Give the extent of all uninfected red blood cells.
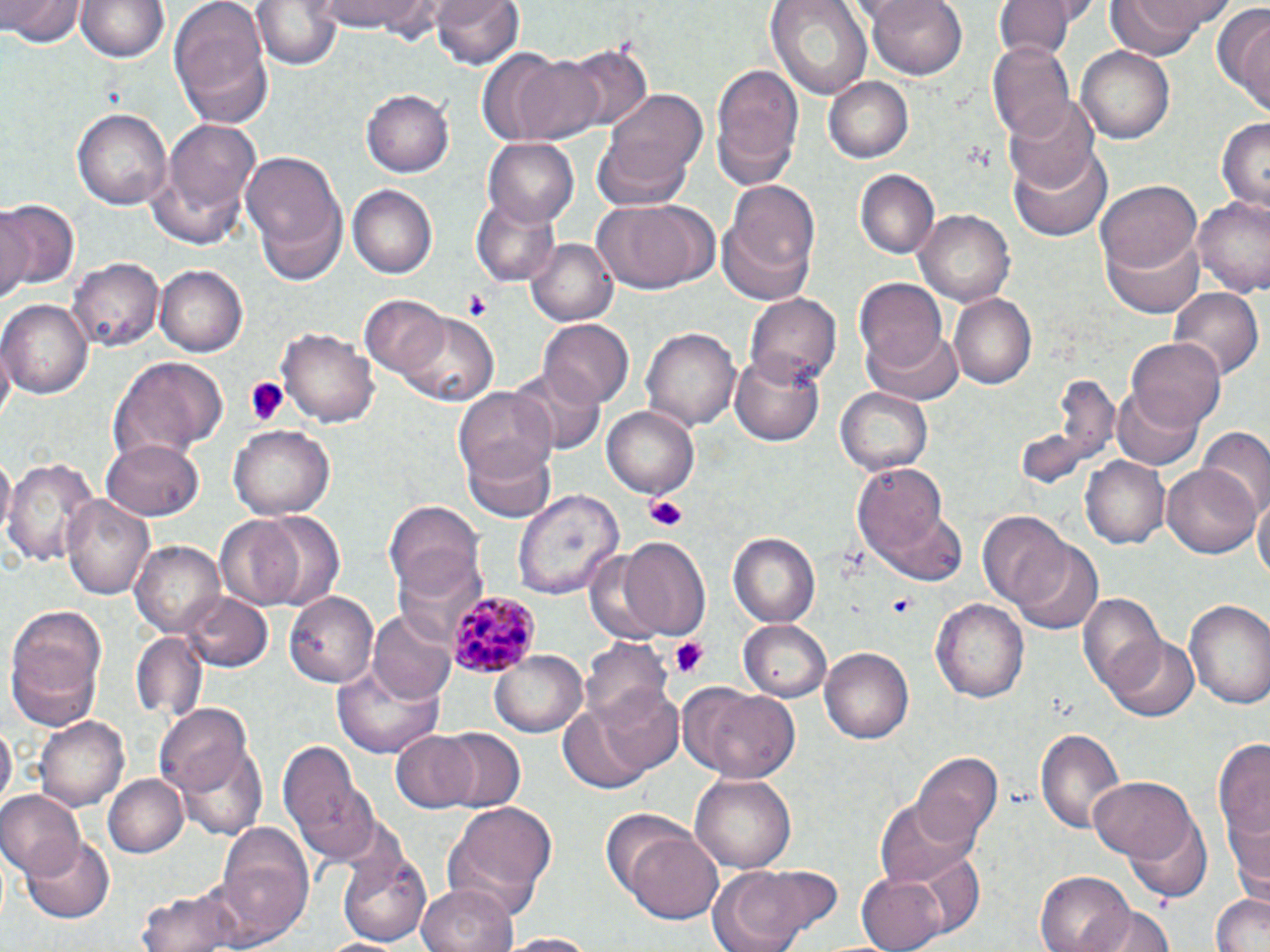
Approximate bounding boxes as (x1, y1, x2, y2) in pixels.
Uninfected red blood cells: (2, 0, 82, 48), (77, 0, 169, 63), (170, 0, 273, 128), (255, 0, 340, 71), (314, 0, 443, 36), (434, 0, 524, 72), (764, 0, 873, 102), (866, 0, 968, 78), (994, 0, 1084, 56), (1105, 0, 1227, 58), (1217, 5, 1270, 114), (989, 39, 1077, 142), (551, 41, 655, 135), (1077, 48, 1176, 145), (506, 52, 603, 144), (711, 59, 803, 189), (823, 77, 912, 162), (362, 90, 453, 176), (595, 90, 707, 204), (1004, 98, 1098, 192), (72, 105, 172, 208), (148, 117, 261, 245), (1217, 118, 1270, 211), (484, 137, 580, 226), (1009, 146, 1111, 242), (241, 147, 345, 274), (855, 168, 939, 258), (716, 180, 824, 305), (1097, 180, 1202, 278), (347, 184, 436, 279), (471, 195, 562, 286), (590, 198, 717, 293), (1193, 198, 1270, 296), (0, 199, 79, 294), (914, 208, 1015, 304), (1104, 227, 1205, 316), (527, 235, 620, 327), (70, 259, 163, 352), (155, 265, 246, 355), (853, 278, 947, 372), (1168, 284, 1262, 382), (744, 292, 844, 388), (948, 294, 1036, 389), (359, 296, 451, 381), (1, 298, 92, 399), (395, 312, 497, 404), (540, 320, 634, 406), (865, 324, 966, 404), (277, 325, 380, 429), (641, 326, 740, 431), (1129, 336, 1226, 432), (730, 351, 824, 445), (109, 356, 227, 460), (512, 368, 605, 456), (1015, 370, 1122, 492), (1112, 384, 1204, 469), (834, 385, 934, 475), (454, 386, 557, 482), (603, 405, 702, 499), (228, 425, 335, 519), (1198, 429, 1270, 519), (463, 438, 559, 524), (104, 439, 202, 520), (1, 454, 15, 536), (1083, 455, 1170, 549), (5, 456, 98, 566), (851, 462, 954, 576), (1162, 465, 1259, 559), (514, 489, 621, 601), (1255, 492, 1270, 586), (64, 493, 155, 601), (385, 502, 485, 604), (246, 509, 347, 609), (977, 513, 1074, 612), (212, 514, 308, 611), (728, 531, 819, 627), (1006, 534, 1102, 635), (617, 537, 709, 639), (133, 542, 226, 639), (182, 592, 272, 672), (286, 592, 383, 685), (1075, 592, 1166, 697), (931, 599, 1029, 703), (1183, 599, 1270, 709), (6, 605, 107, 712), (369, 608, 457, 702), (739, 618, 833, 699), (131, 632, 206, 723), (1105, 634, 1197, 721), (580, 636, 671, 724), (819, 646, 913, 746), (488, 649, 590, 738), (9, 650, 100, 731), (331, 656, 447, 758), (593, 684, 687, 775), (682, 686, 800, 782), (155, 705, 254, 797), (559, 705, 655, 793), (36, 716, 129, 809), (0, 722, 14, 807), (1033, 726, 1128, 836), (438, 728, 527, 814), (1212, 733, 1270, 877), (392, 734, 479, 813), (172, 735, 272, 843), (275, 741, 378, 862), (912, 752, 1003, 851), (104, 773, 188, 859), (689, 773, 798, 874), (1089, 776, 1196, 864), (0, 792, 84, 879), (874, 794, 977, 888), (1224, 801, 1270, 895), (444, 803, 559, 916), (598, 809, 694, 896), (1126, 814, 1211, 903), (215, 824, 314, 941), (625, 831, 725, 925), (23, 834, 114, 922), (338, 848, 432, 946), (738, 863, 847, 942), (705, 869, 811, 952), (858, 871, 953, 952), (1037, 872, 1134, 952), (417, 882, 518, 952), (138, 885, 249, 952), (1211, 893, 1270, 952), (1092, 906, 1174, 952), (498, 932, 602, 951), (319, 935, 405, 952).

slide-level diagnosis = Plasmodium malariae
field of view = single
preparation = thin blood smear
image size = 1270×952 pixels
stain = May-Grünwald-Giemsa
Plasmodium malariae-infected red blood cell locations = approximate bounding boxes as (x1, y1, x2, y2) in pixels: (446, 589, 538, 676)
modality = optical microscopy
platelet locations = approximate bounding boxes as (x1, y1, x2, y2) in pixels: (462, 291, 490, 319), (240, 378, 290, 429), (642, 493, 692, 530), (887, 593, 917, 615), (669, 636, 712, 679)
magnification = 1000x